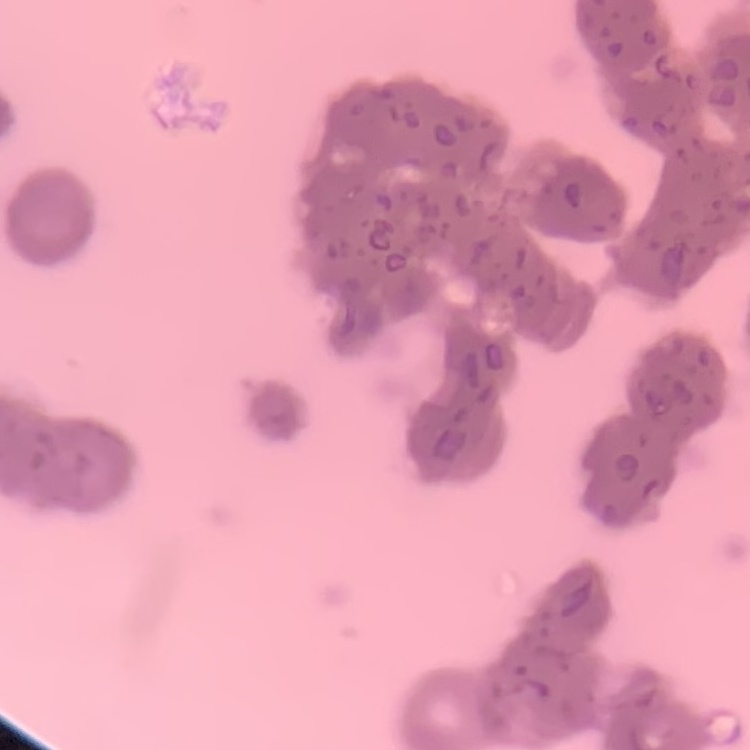
The erythrocytes show rouleaux formation. One tile cut from a larger photomicrograph. Thin peripheral smear. Stained with either Field's or Giemsa.